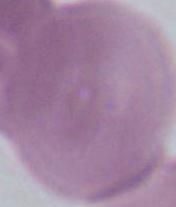

Captured at 1000x magnification. Photomicrograph. A red blood cell is shown.